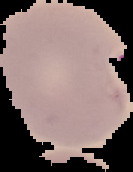

Summary:
  - Result: malaria parasites identified
  - Image size: 133×172 pixels
  - Preparation: thin blood smear
  - Image type: segmented cell region with the area outside set to black